Identify the cell.
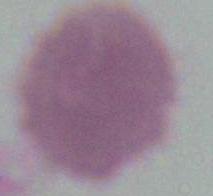
This is an erythrocyte.

{
  "magnification": "1000x",
  "modality": "photomicrograph"
}